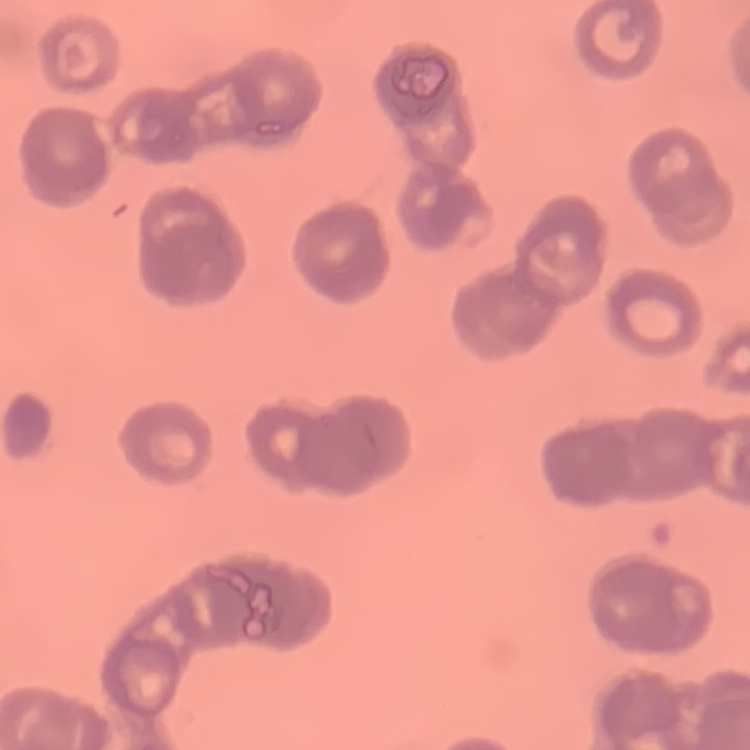

red blood cell morphology = rouleaux formation
stain = Field's or Giemsa
preparation = thin blood smear
image type = one tile cut from a larger photomicrograph